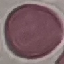
Summary:
  - Malaria status: uninfected
  - Stain: Giemsa
  - Image type: automatically extracted cell patch, resized to 64 × 64 pixels
  - Capture: smartphone camera at the microscope eyepiece
  - Preparation: thin blood smear